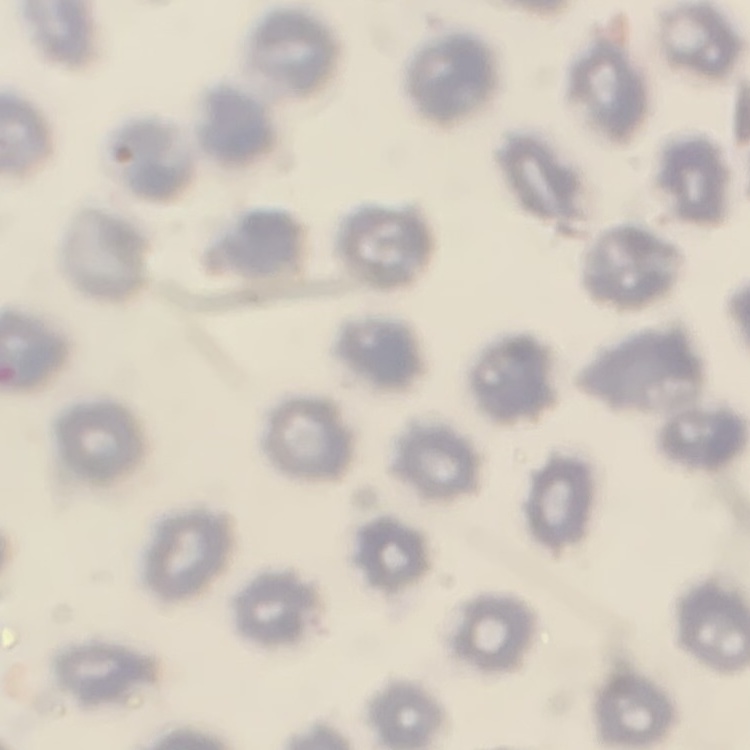

Summary:
  - Erythrocyte morphology: no rouleaux formation
  - Preparation: thin blood smear
  - Stain: Field's or Giemsa
  - Image type: one tile cut from a larger photomicrograph